State the blood parasite species.
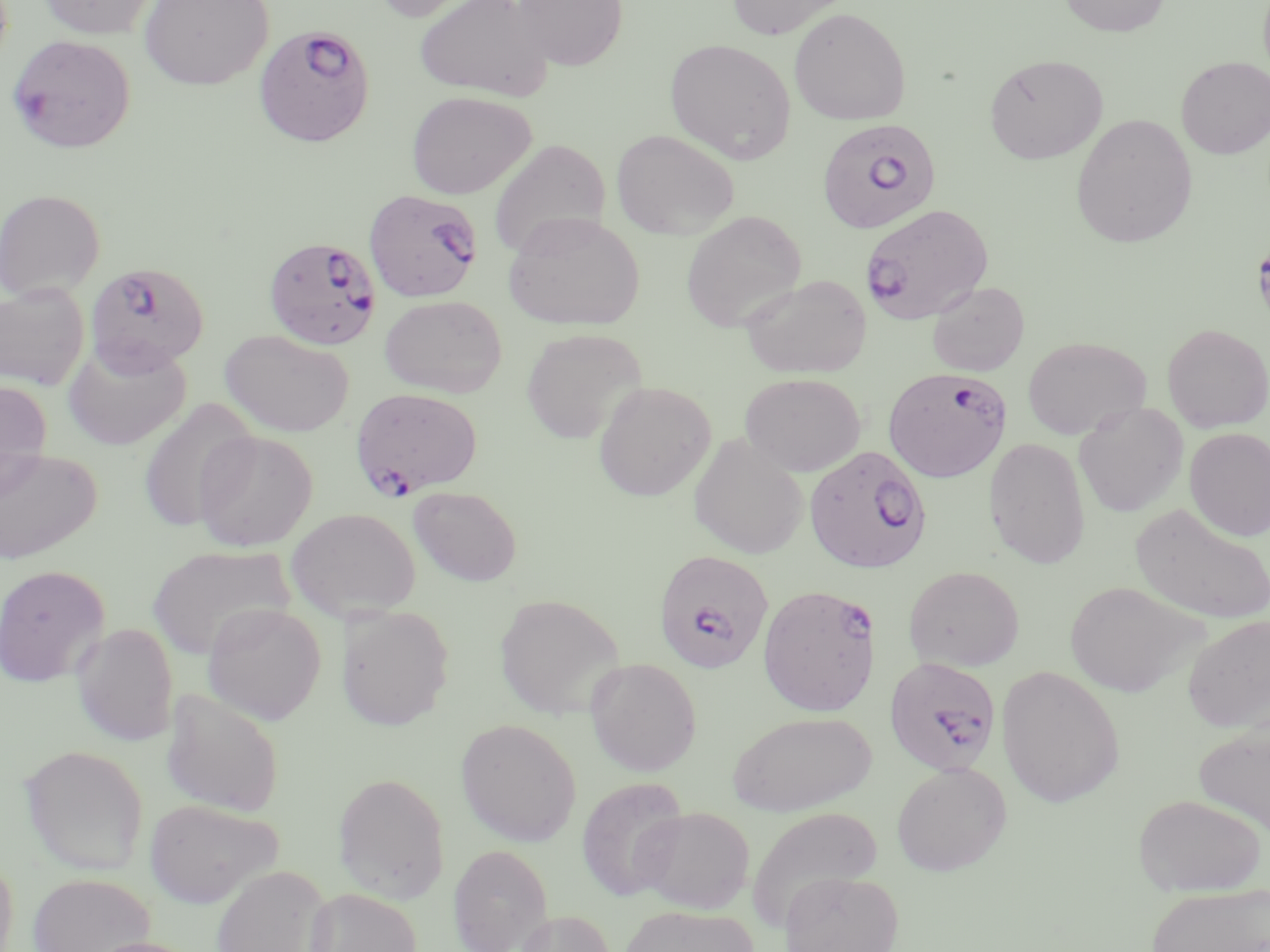

Plasmodium falciparum.

Approximate bounding boxes as [x1, y1, x2, y2] in pixels. Uninfected red blood cell locations: [37, 0, 159, 39], [137, 0, 274, 91], [369, 0, 493, 23], [413, 0, 555, 101], [511, 0, 628, 71], [726, 0, 851, 39], [1059, 0, 1171, 37], [789, 7, 911, 125], [665, 38, 796, 163], [984, 54, 1108, 164], [1176, 57, 1270, 159], [406, 91, 536, 199], [1070, 113, 1198, 248], [611, 129, 739, 240], [488, 138, 611, 259], [0, 188, 106, 302], [681, 211, 807, 332], [503, 212, 645, 331], [739, 274, 873, 378], [926, 281, 1030, 376], [0, 283, 90, 391], [379, 294, 507, 398], [1162, 323, 1270, 432], [521, 328, 647, 444], [220, 329, 355, 438], [1022, 336, 1150, 440], [62, 339, 191, 451], [739, 372, 866, 477], [0, 380, 53, 497], [593, 380, 716, 501], [137, 397, 257, 533], [1074, 402, 1188, 517], [1184, 427, 1270, 541], [193, 430, 318, 551], [688, 433, 809, 559], [983, 437, 1091, 569], [0, 447, 101, 565], [409, 486, 522, 586], [1130, 503, 1269, 625], [286, 507, 421, 621], [147, 545, 296, 659], [0, 565, 110, 687], [903, 565, 1025, 672], [1063, 580, 1205, 697], [494, 593, 625, 720], [202, 601, 326, 725], [337, 605, 454, 731], [1183, 615, 1270, 733], [71, 622, 178, 747], [585, 658, 703, 776], [996, 665, 1125, 808], [161, 688, 285, 818], [727, 711, 876, 817], [456, 719, 581, 847], [1193, 719, 1270, 836], [19, 744, 149, 874], [891, 762, 1010, 876], [333, 772, 451, 902], [575, 776, 688, 901], [1132, 794, 1266, 896], [144, 798, 283, 908], [747, 805, 887, 930], [635, 806, 754, 914], [448, 843, 552, 952], [0, 852, 20, 952], [210, 865, 333, 952], [779, 871, 904, 952], [28, 873, 155, 952], [1144, 882, 1270, 952], [305, 887, 422, 952], [619, 905, 757, 952], [514, 909, 618, 952], [80, 936, 204, 952]. Plasmodium falciparum-infected red blood cell locations: [253, 24, 376, 148], [6, 33, 136, 154], [817, 118, 941, 234], [363, 189, 483, 303], [858, 203, 994, 324], [263, 235, 382, 350], [85, 261, 210, 373], [884, 366, 1011, 482], [350, 387, 483, 498], [804, 445, 932, 574], [652, 549, 774, 673], [758, 583, 881, 717], [883, 657, 1000, 775]. Image is 1270×952 pixels. Thin blood smear. One field of a larger specimen. 1000x magnification. May-Grünwald-Giemsa stain. Optical microscopy.